Classify this cell by malaria status.
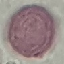

Uninfected.

image type = cell patch, automatically extracted from a larger field of view and resized to 64 × 64 pixels
preparation = thin blood film
capture = smartphone camera at the microscope eyepiece
stain = Giemsa